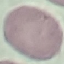
malaria_status: uninfected
image_type: cell patch, automatically extracted from a larger field of view and resized to 64 × 64 pixels
preparation: thin smear
stain: Giemsa
capture: smartphone camera at the microscope eyepiece